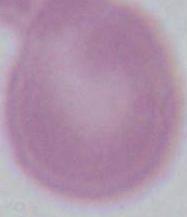

identification: erythrocyte
magnification: 1000x
modality: photomicrograph